Report the malaria status.
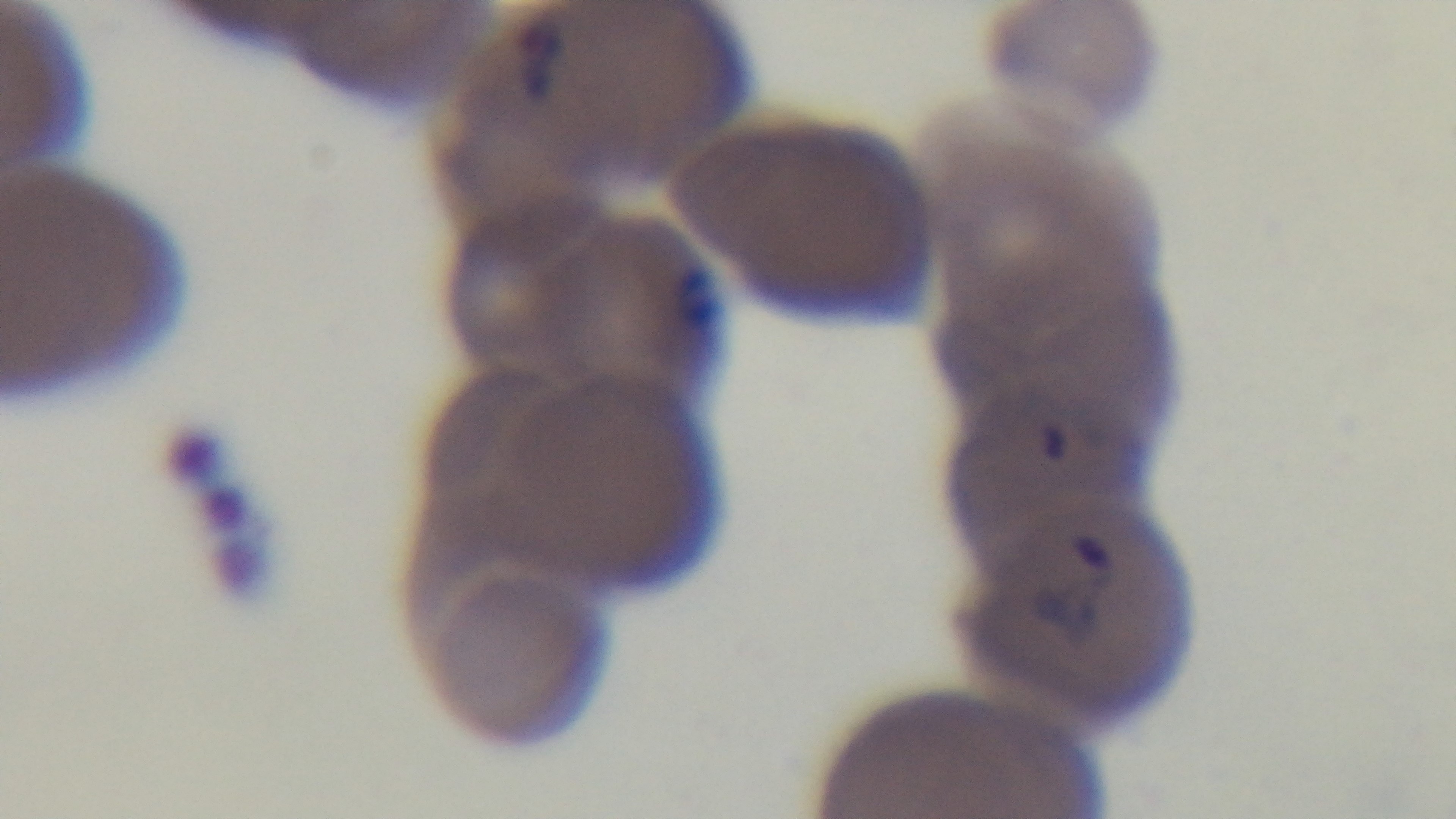

It is infected.

Light microscopy. Mounted 4K digital camera. 100x oil-immersion objective. Single field of view. Giemsa-stained. Preparation: thin blood film.